State the blood parasite species.
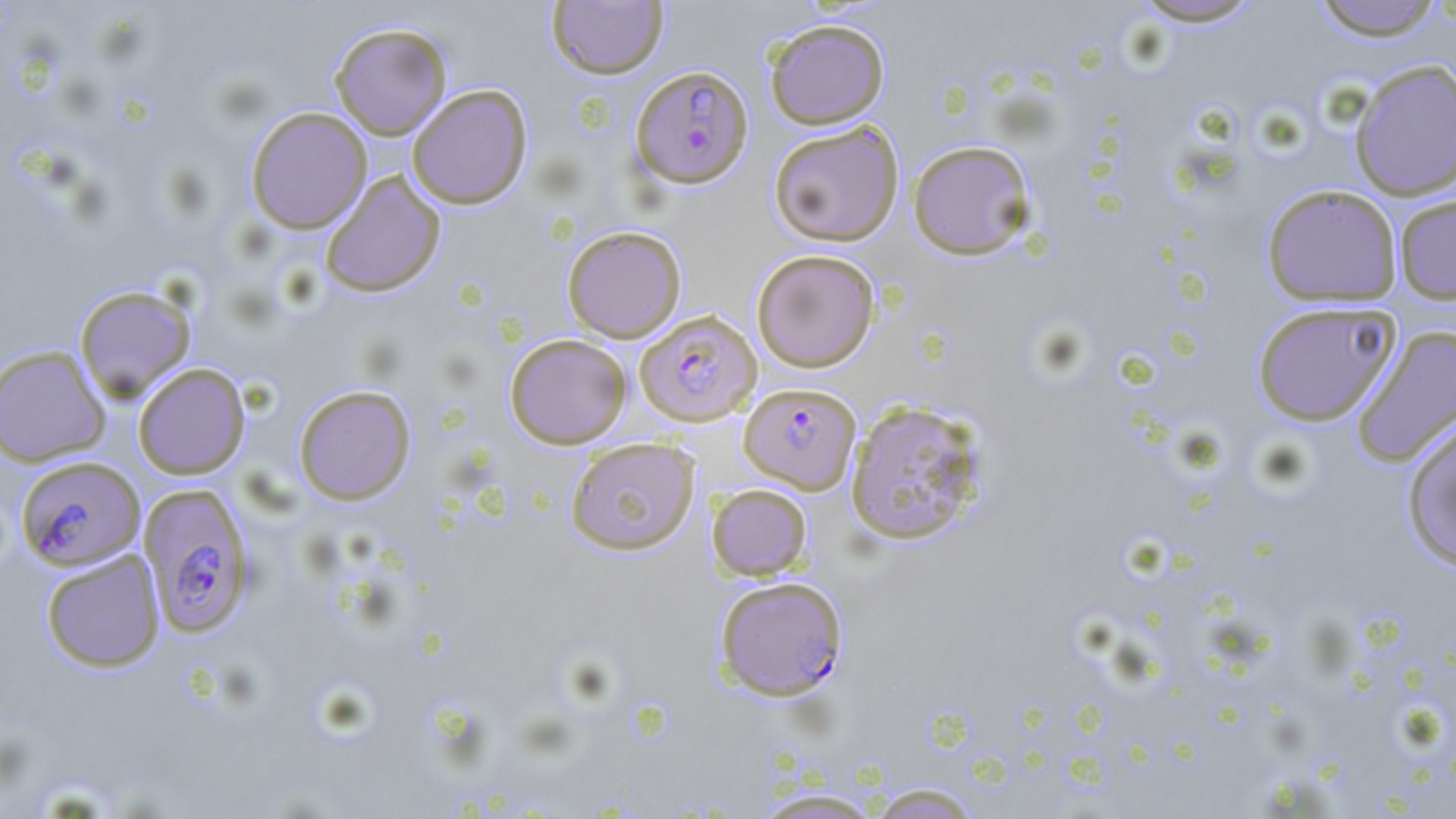

Plasmodium falciparum.

Approximate bounding boxes as (x1,y1)-(x2,y2) corner pairs in pixels. Plasmodium falciparum-infected red blood cell locations: (631,65)-(753,188), (635,309)-(762,426), (739,382)-(860,494), (15,455)-(145,570), (138,483)-(256,638), (714,575)-(849,702). Uninfected red blood cell locations: (1309,0)-(1447,41), (546,1)-(668,79), (1127,1)-(1269,28), (764,19)-(889,129), (329,22)-(452,139), (1348,59)-(1456,201), (406,84)-(533,209), (245,106)-(372,234), (768,121)-(904,247), (907,140)-(1037,260), (320,171)-(446,298), (1261,184)-(1403,307), (1394,194)-(1456,305), (562,225)-(687,343), (751,249)-(880,372), (74,285)-(196,401), (1251,301)-(1401,427), (1351,324)-(1456,469), (505,333)-(631,449), (0,344)-(111,466), (133,362)-(250,479), (293,384)-(416,505), (844,399)-(987,546), (1400,417)-(1456,573), (566,437)-(700,555), (707,484)-(812,581), (40,549)-(164,672), (867,783)-(983,818), (751,788)-(886,818). Single field of view. 1000x magnification. Thin blood smear. May-Grünwald-Giemsa-stained preparation. Image is 1456×819 pixels. Optical microscopy.